Locate and identify every blood parasite.
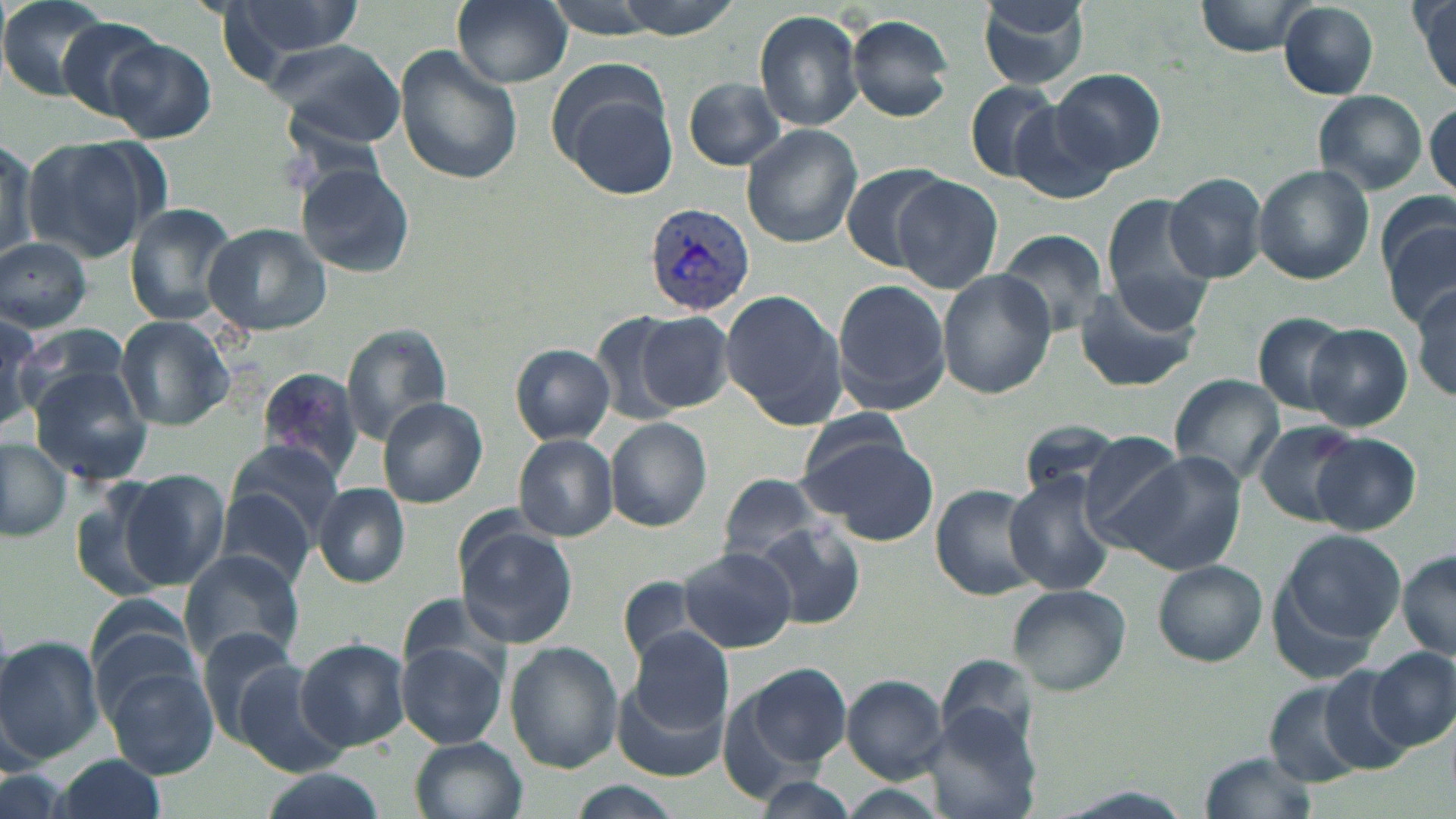
Approximate bounding boxes as [x1, y1, x2, y2] in pixels.
Plasmodium vivax-infected red blood cells: [644, 200, 756, 313].
No Plasmodium falciparum, Plasmodium ovale, Plasmodium malariae, Babesia divergens, or Trypanosoma brucei observed.

{
  "slide_level_diagnosis": "Plasmodium vivax",
  "magnification": "1000x",
  "image_size": "1456×819 pixels",
  "preparation": "thin blood film",
  "uninfected_red_blood_cell_locations": "approximate bounding boxes as [x1, y1, x2, y2] in pixels: [215, 0, 366, 77], [453, 0, 572, 88], [532, 0, 680, 37], [978, 0, 1092, 89], [1192, 0, 1315, 57], [0, 1, 120, 103], [1414, 2, 1456, 96], [1279, 4, 1379, 99], [755, 9, 865, 131], [845, 15, 955, 121], [58, 17, 168, 123], [104, 37, 216, 144], [265, 38, 408, 150], [397, 46, 523, 186], [548, 60, 677, 191], [1051, 68, 1166, 177], [684, 77, 788, 171], [963, 79, 1064, 183], [1313, 90, 1427, 195], [1426, 96, 1455, 198], [1008, 104, 1116, 206], [742, 124, 863, 248], [23, 137, 154, 263], [0, 138, 37, 268], [839, 162, 952, 271], [296, 164, 412, 276], [1253, 165, 1374, 285], [1164, 173, 1268, 283], [893, 175, 1003, 293], [1102, 194, 1216, 330], [125, 203, 238, 325], [1383, 209, 1456, 328], [204, 223, 330, 338], [995, 229, 1111, 338], [0, 237, 92, 333], [937, 270, 1057, 398], [832, 279, 952, 414], [1071, 283, 1199, 393], [1410, 286, 1456, 402], [720, 289, 847, 430], [0, 310, 42, 431], [637, 310, 735, 413], [1251, 312, 1351, 417], [590, 314, 695, 426], [115, 315, 233, 430], [19, 324, 132, 407], [1304, 324, 1411, 432], [341, 325, 453, 443], [512, 344, 614, 443], [28, 368, 151, 486], [257, 368, 365, 479], [1169, 374, 1283, 486], [378, 397, 489, 508], [606, 418, 713, 532], [1017, 421, 1129, 504], [1256, 421, 1358, 523], [801, 430, 939, 544], [513, 433, 617, 541], [1311, 434, 1421, 535], [1079, 435, 1193, 546], [0, 437, 72, 540], [225, 439, 345, 545], [1120, 452, 1246, 576], [120, 469, 230, 590], [716, 473, 829, 565], [1006, 474, 1116, 597], [313, 484, 409, 587], [932, 484, 1050, 601], [73, 487, 171, 602], [217, 489, 318, 588], [455, 518, 580, 648], [754, 520, 869, 630], [1271, 529, 1409, 660], [679, 546, 796, 654], [1399, 549, 1455, 661], [180, 550, 306, 667], [1154, 561, 1267, 666], [617, 576, 711, 669], [1007, 587, 1131, 696], [86, 599, 206, 714], [630, 627, 733, 735], [196, 629, 312, 748], [0, 635, 104, 763], [294, 638, 409, 751], [398, 640, 506, 748], [507, 642, 621, 772], [1367, 647, 1456, 752], [98, 660, 220, 780], [743, 660, 851, 770], [233, 664, 348, 776], [1319, 667, 1419, 773], [613, 675, 729, 782], [843, 675, 948, 781], [1263, 675, 1379, 785], [411, 735, 529, 819], [53, 753, 169, 819], [1202, 753, 1316, 817], [253, 769, 390, 819], [753, 776, 863, 817], [565, 783, 685, 819], [829, 785, 954, 817]",
  "field_of_view": "single",
  "modality": "light microscopy",
  "stain": "May-Grünwald-Giemsa"
}